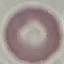
{
  "result": "negative for malaria parasites",
  "preparation": "thin smear",
  "image_type": "automatically extracted cell patch, resized to 64 × 64 pixels",
  "capture": "smartphone camera at the microscope eyepiece",
  "stain": "Giemsa"
}